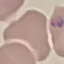

Malaria status: parasitized. Cell patch, automatically extracted from a larger field of view and resized to 64 × 64 pixels. Giemsa stain. Photographed with a smartphone camera at the microscope eyepiece. Thin blood film.